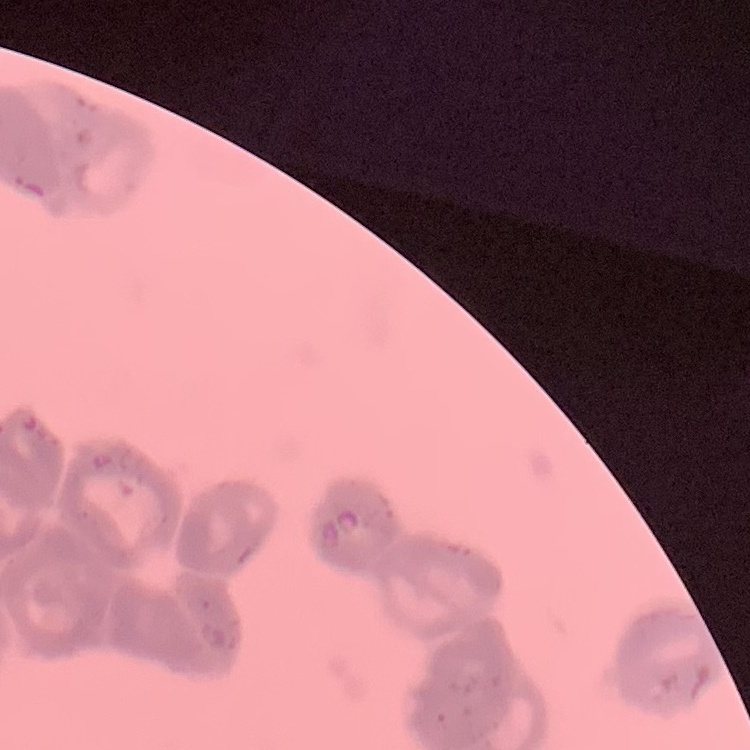 The erythrocytes show rouleaux formation. Stained with either Field's or Giemsa. Thin peripheral smear. One tile cut from a larger photomicrograph.